Locate every Plasmodium parasite.
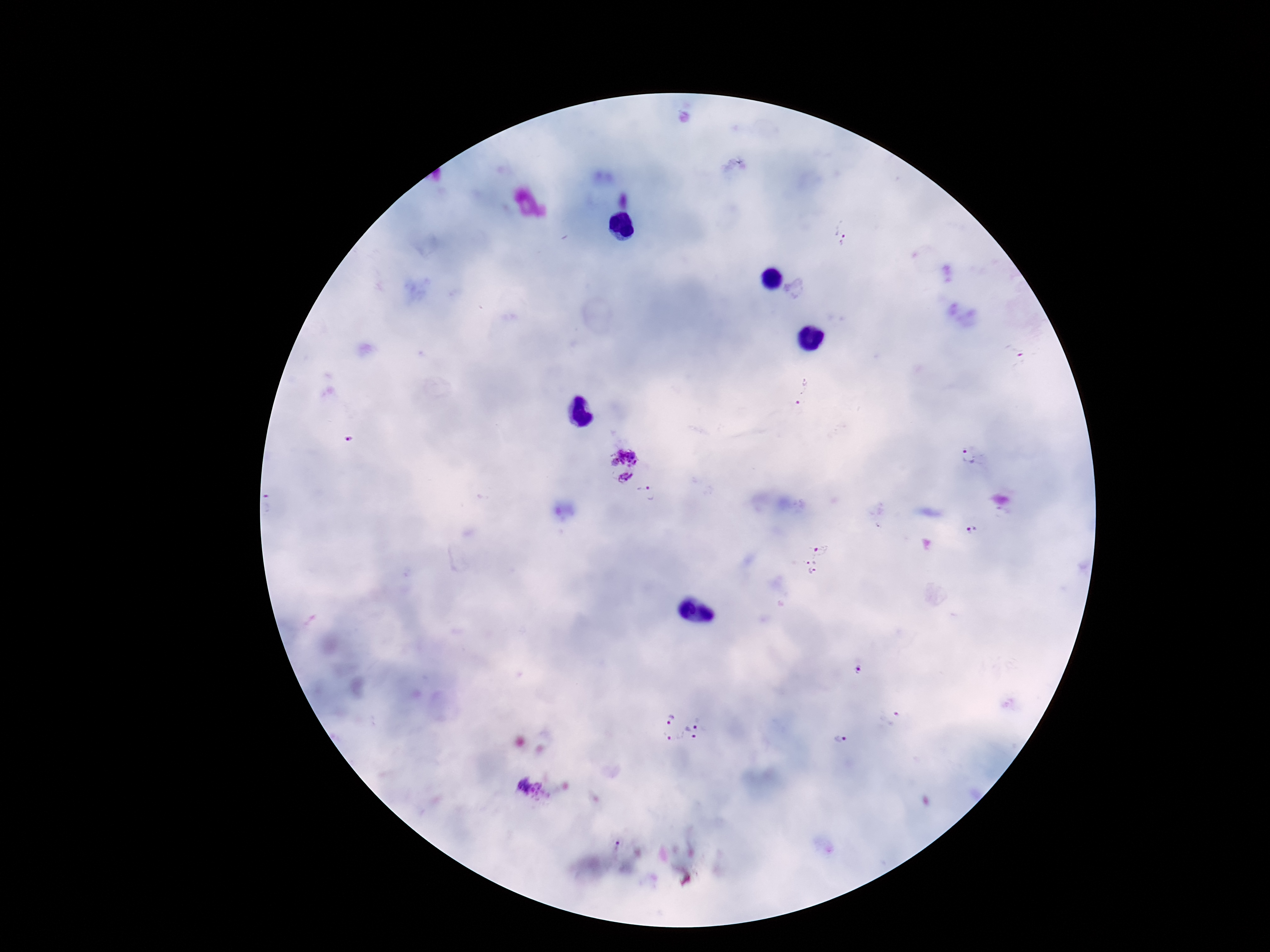

Approximate centers as [x, y] in pixels.
Plasmodium parasites: [843, 233], [805, 392], [969, 458], [623, 466], [973, 528], [816, 562], [894, 719], [682, 726], [843, 739], [533, 789].

Thick blood smear. 100x magnification. One field from this slide. Giemsa stain. Smartphone photograph taken through the microscope eyepiece. Patient malaria status: infected. Image is 1270×952 pixels.